Classify this cell by malaria status.
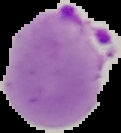
It is parasitized.

preparation = thin blood film
image type = segmented cell region on a black background
image size = 121×133 pixels